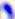
Micrograph. 400x magnification. Toxoplasma gondii is seen.